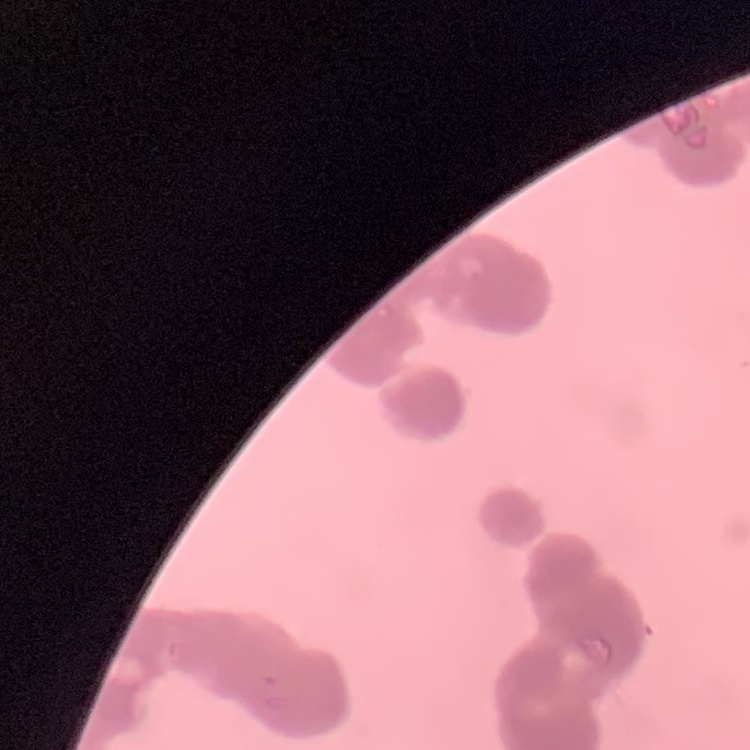
The erythrocytes show rouleaux formation. Stained with either Field's or Giemsa. Square crop of a larger photomicrograph. Thin blood smear.